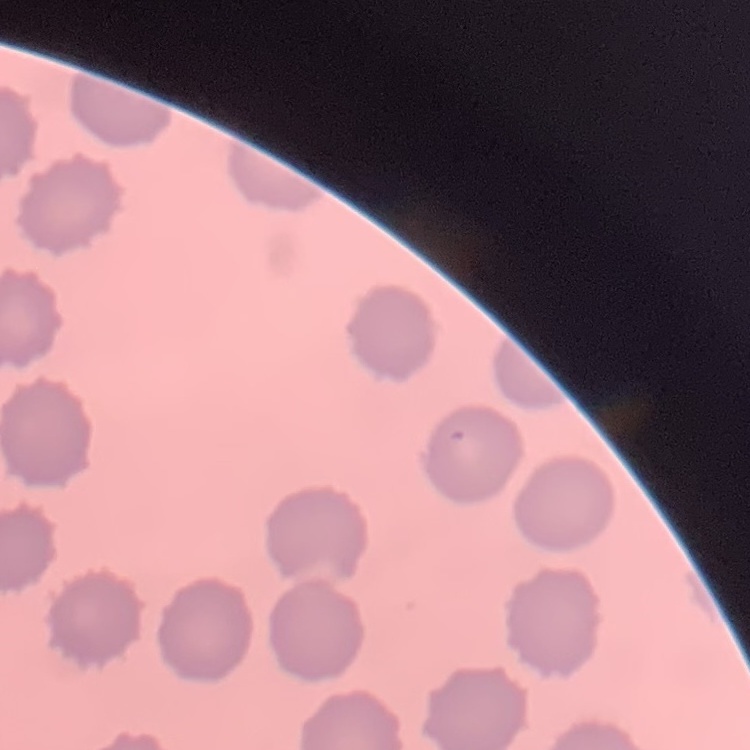
erythrocyte morphology = no rouleaux formation
stain = Field's or Giemsa
image type = one tile cut from a larger photomicrograph
preparation = thin blood film